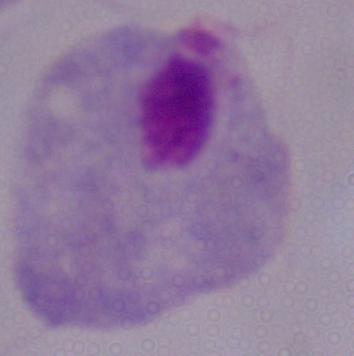

magnification = 1000x
identification = trichomonad
modality = micrograph